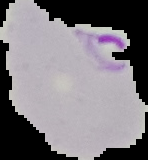

Summary:
  - Image type: cell region segmented out of the field of view; surrounding area masked to black
  - Image size: 148×160 pixels
  - Result: malaria parasites detected
  - Preparation: thin blood film